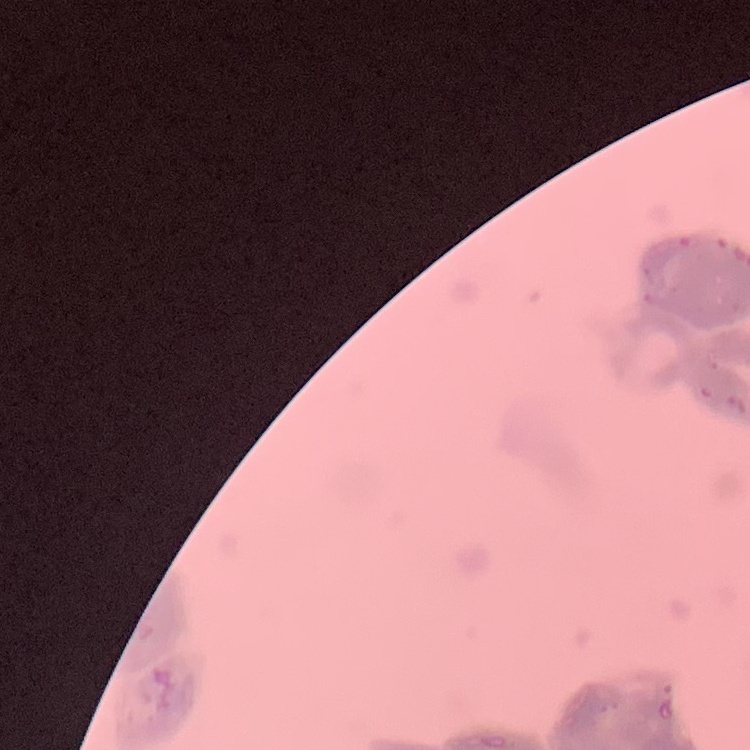 The erythrocytes exhibit rouleaux formation. Stained with either Field's or Giemsa. Square crop of a larger photomicrograph. Thin blood film.